Give the position of every Plasmodium parasite.
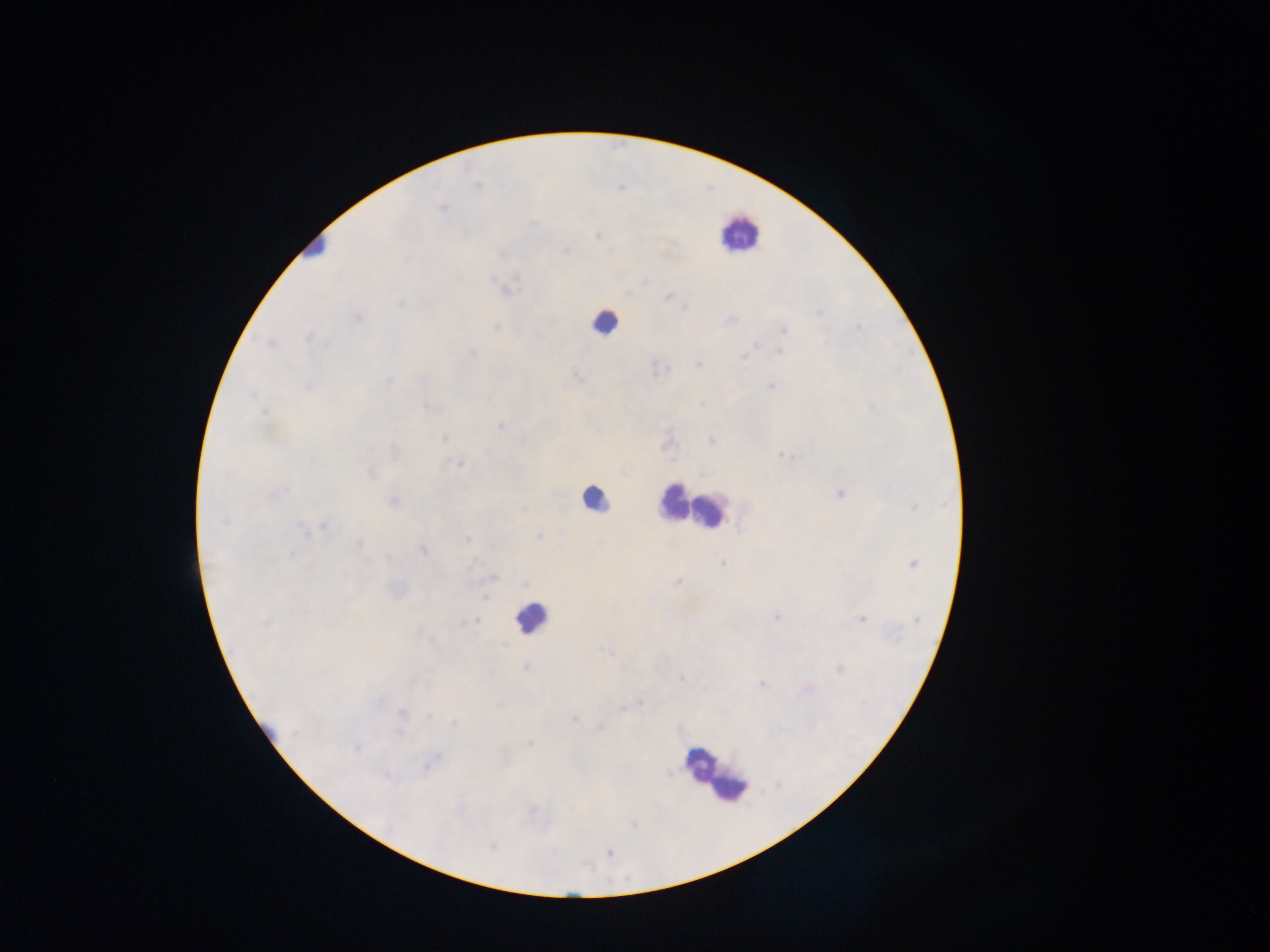

Approximate centers as {x, y} in pixels.
Plasmodium parasites: {441, 208}, {597, 236}, {567, 252}, {502, 254}, {506, 289}, {668, 297}, {401, 303}, {685, 308}, {819, 312}, {357, 318}, {731, 320}, {495, 326}, {858, 328}, {783, 330}, {309, 337}, {782, 340}, {270, 343}, {755, 344}, {780, 351}, {473, 353}, {744, 357}, {699, 365}, {657, 368}, {578, 378}, {389, 381}, {309, 386}, {771, 387}, {700, 404}, {428, 407}, {264, 412}, {500, 426}, {444, 438}, {711, 440}, {668, 441}, {785, 456}, {459, 464}, {371, 473}, {277, 493}, {839, 493}, {394, 501}, {913, 508}, {523, 510}, {323, 526}, {300, 528}, {538, 536}, {468, 539}, {358, 546}, {421, 549}, {290, 555}, {474, 562}, {722, 563}, {914, 564}, {493, 577}, {677, 582}, {486, 598}, {612, 610}, {776, 617}, {860, 619}, {477, 621}, {918, 621}, {469, 622}, {266, 623}, {504, 645}, {604, 652}, {525, 668}, {682, 679}, {763, 685}, {379, 701}, {640, 703}, {621, 709}, {402, 714}, {429, 716}, {574, 719}, {455, 723}, {600, 727}, {295, 733}, {401, 734}, {530, 744}, {355, 749}, {428, 765}, {388, 778}, {491, 846}, {609, 853}.

preparation = thick blood film
capture = mobile-phone photograph through a microscope
country = Ghana
field of view = single
image size = 1270×952 pixels
leukocyte locations = approximate centers as {x, y} in pixels: {738, 233}, {315, 246}, {603, 322}, {594, 499}, {672, 501}, {711, 511}, {531, 618}, {700, 765}, {732, 788}